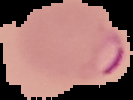

Image is 133×100 pixels. Result: malaria parasites identified. Cell region segmented out of the field of view; the surrounding area is masked to black. From a thin blood film.